Assess this cell for malaria.
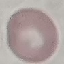

Uninfected.

Summary:
  - Capture: smartphone through the microscope eyepiece
  - Image type: automatically extracted cell patch, resized to 64 × 64 pixels
  - Preparation: thin blood film
  - Stain: Giemsa